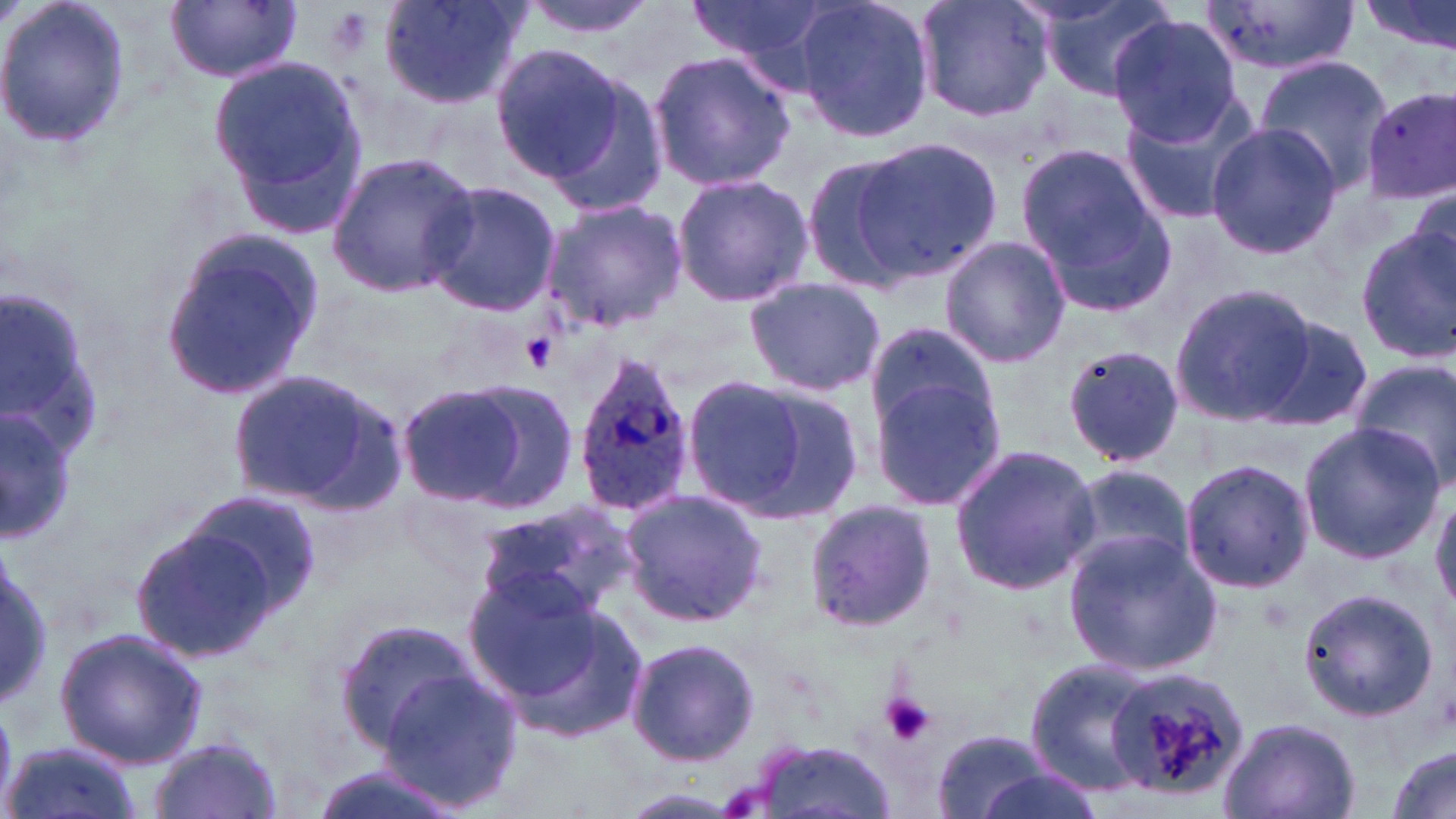

Summary:
  - Coordinate format: approximate bounding boxes as named x1/y1/x2/y2 corners in pixels
  - Uninfected red blood cell locations: (x1=0, y1=0, x2=132, y2=152), (x1=376, y1=0, x2=531, y2=107), (x1=516, y1=0, x2=663, y2=39), (x1=684, y1=0, x2=842, y2=80), (x1=791, y1=0, x2=935, y2=144), (x1=915, y1=0, x2=1054, y2=123), (x1=1358, y1=0, x2=1455, y2=61), (x1=164, y1=1, x2=302, y2=84), (x1=1035, y1=1, x2=1181, y2=99), (x1=1195, y1=1, x2=1358, y2=76), (x1=1108, y1=15, x2=1244, y2=145), (x1=489, y1=42, x2=627, y2=181), (x1=645, y1=47, x2=796, y2=194), (x1=208, y1=53, x2=375, y2=238), (x1=1254, y1=57, x2=1391, y2=193), (x1=530, y1=65, x2=672, y2=216), (x1=1361, y1=86, x2=1455, y2=206), (x1=1118, y1=94, x2=1259, y2=227), (x1=1206, y1=123, x2=1340, y2=261), (x1=842, y1=137, x2=1002, y2=286), (x1=1016, y1=141, x2=1174, y2=312), (x1=324, y1=152, x2=479, y2=299), (x1=798, y1=152, x2=922, y2=291), (x1=671, y1=172, x2=815, y2=308), (x1=423, y1=179, x2=562, y2=320), (x1=1407, y1=184, x2=1455, y2=283), (x1=541, y1=198, x2=687, y2=334), (x1=1355, y1=228, x2=1456, y2=360), (x1=159, y1=229, x2=328, y2=399), (x1=938, y1=235, x2=1068, y2=369), (x1=742, y1=277, x2=886, y2=395), (x1=1170, y1=283, x2=1317, y2=426), (x1=1258, y1=315, x2=1377, y2=431), (x1=864, y1=323, x2=999, y2=448), (x1=1059, y1=344, x2=1187, y2=471), (x1=1348, y1=357, x2=1456, y2=493), (x1=227, y1=370, x2=400, y2=510), (x1=870, y1=371, x2=1012, y2=514), (x1=689, y1=375, x2=865, y2=523), (x1=450, y1=378, x2=580, y2=513), (x1=392, y1=383, x2=533, y2=508), (x1=0, y1=404, x2=79, y2=542), (x1=1297, y1=420, x2=1446, y2=564), (x1=949, y1=442, x2=1100, y2=596), (x1=1178, y1=458, x2=1315, y2=595), (x1=1059, y1=463, x2=1196, y2=579), (x1=178, y1=487, x2=324, y2=622), (x1=617, y1=489, x2=769, y2=629), (x1=1431, y1=490, x2=1456, y2=617), (x1=802, y1=499, x2=937, y2=634), (x1=475, y1=500, x2=637, y2=622), (x1=125, y1=521, x2=287, y2=665), (x1=1061, y1=530, x2=1222, y2=676), (x1=0, y1=546, x2=50, y2=713), (x1=465, y1=577, x2=640, y2=737), (x1=1295, y1=586, x2=1442, y2=724), (x1=332, y1=617, x2=480, y2=755), (x1=54, y1=628, x2=207, y2=768), (x1=625, y1=636, x2=761, y2=767), (x1=1024, y1=656, x2=1160, y2=794), (x1=376, y1=667, x2=524, y2=811), (x1=1215, y1=716, x2=1361, y2=819), (x1=928, y1=727, x2=1060, y2=819), (x1=146, y1=735, x2=286, y2=819), (x1=750, y1=739, x2=897, y2=819), (x1=3, y1=740, x2=146, y2=819), (x1=1384, y1=747, x2=1455, y2=819), (x1=302, y1=762, x2=468, y2=819), (x1=965, y1=765, x2=1106, y2=819)
  - Platelet locations: (x1=518, y1=333, x2=557, y2=370), (x1=879, y1=694, x2=935, y2=747)
  - Plasmodium ovale-infected red blood cell locations: (x1=570, y1=350, x2=696, y2=522), (x1=1102, y1=668, x2=1247, y2=802)
  - Slide-level diagnosis: Plasmodium ovale
  - Image size: 1456×819 pixels
  - Modality: light microscopy
  - Magnification: 1000x
  - Field of view: one of a larger specimen
  - Preparation: thin blood smear
  - Stain: May-Grünwald-Giemsa